Assess the morphology of the erythrocytes.
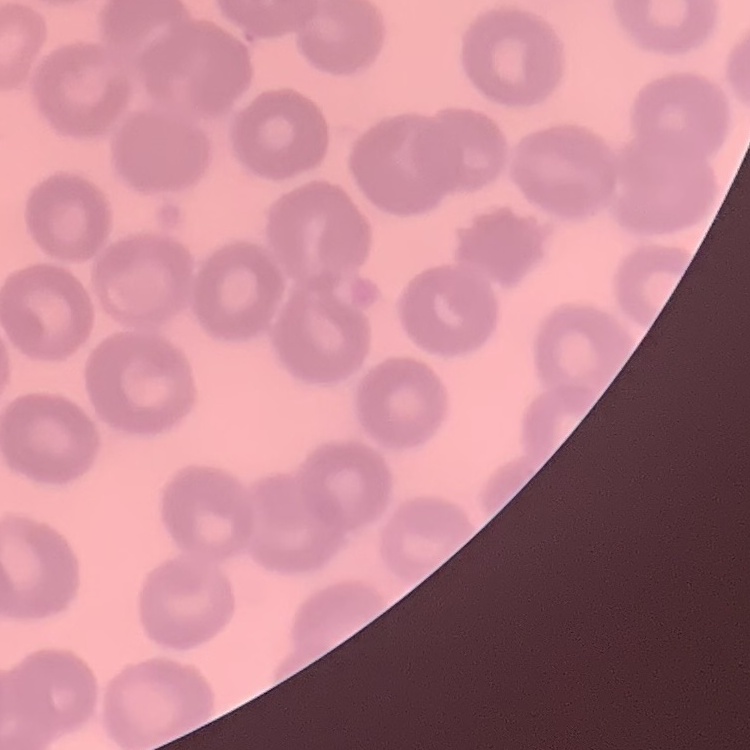

They show no rouleaux formation.

One tile cut from a larger photomicrograph. Stained with either Field's or Giemsa. Thin blood film.